Name the cell type shown.
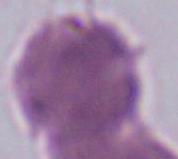
An erythrocyte.

Summary:
  - Magnification: 1000x
  - Modality: photomicrograph